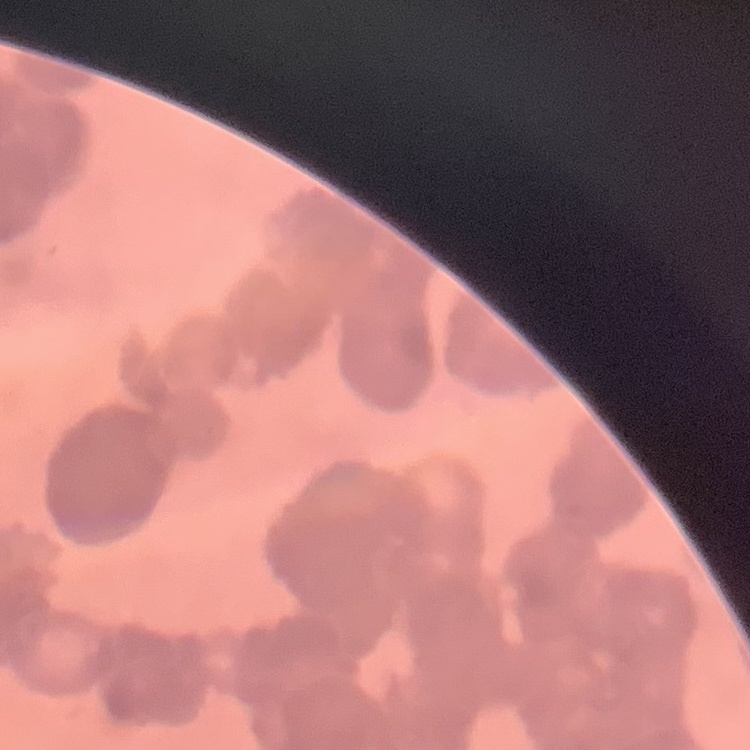
erythrocyte morphology = rouleaux formation
image type = one tile cut from a larger photomicrograph
preparation = thin peripheral smear
stain = Field's or Giemsa